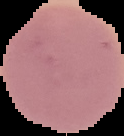

preparation = thin blood film
image size = 124×136 pixels
image type = segmented cell region on a black background
malaria status = uninfected